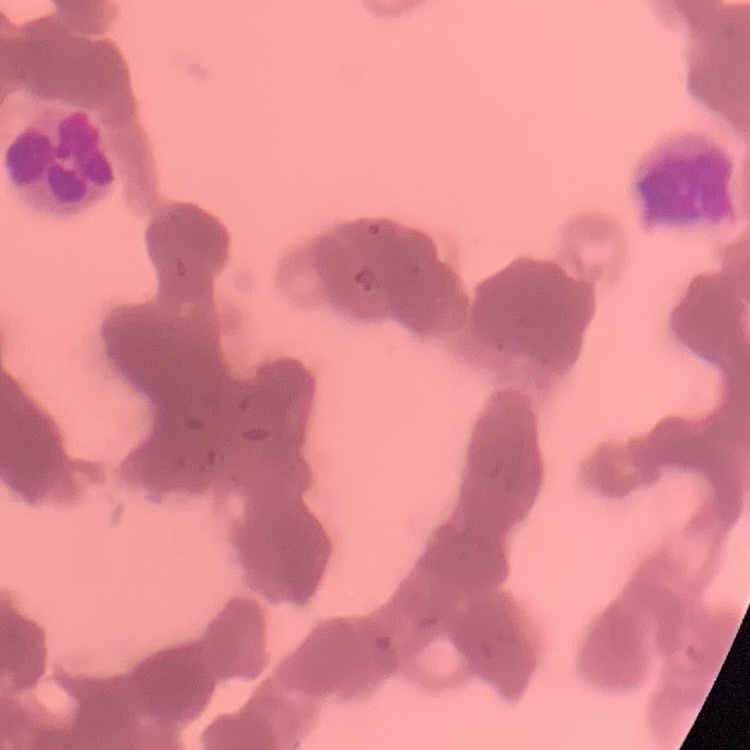

The red blood cells show rouleaux formation. Thin blood smear. Square crop of a larger photomicrograph. Stained with either Field's or Giemsa.